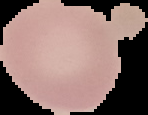

Summary:
  - Image size: 148×115 pixels
  - Result: no Plasmodium parasites detected
  - Preparation: thin blood film
  - Image type: segmented cell region on a black background